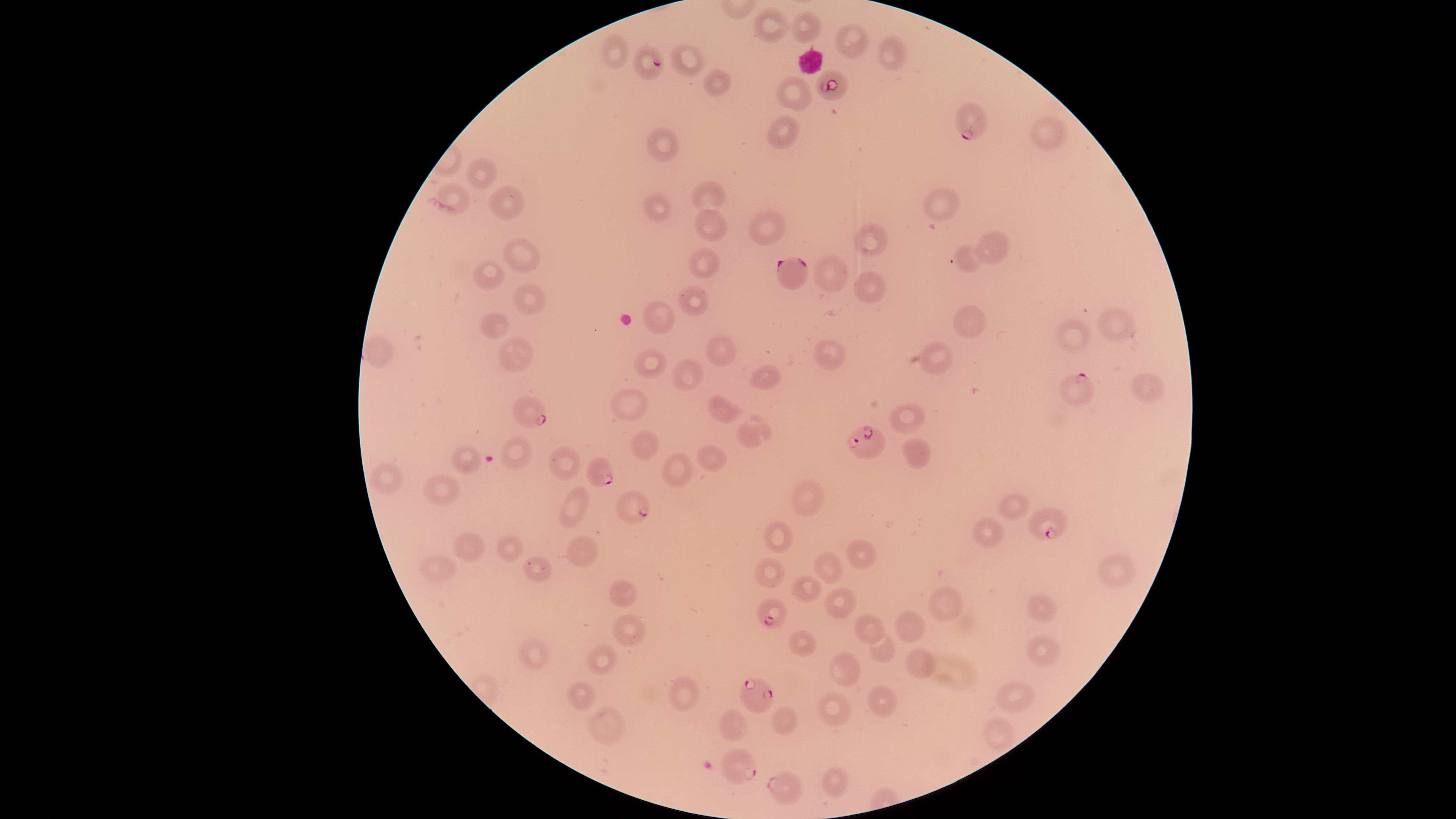
image size = 1456×819 pixels
capture = smartphone photograph through the microscope eyepiece
uninfected RBCs = approximate marker points as [x, y] in pixels: [801, 27], [763, 31], [847, 43], [617, 54], [885, 54], [688, 61], [713, 82], [792, 92], [780, 130], [1047, 130], [663, 145], [477, 181], [708, 192], [503, 204], [945, 208], [655, 214], [708, 223], [763, 228], [992, 246], [869, 249], [524, 259], [706, 261], [969, 265], [487, 274], [836, 279], [867, 289], [530, 299], [694, 301], [964, 319], [660, 321], [1106, 329], [497, 330], [1072, 339], [723, 346], [834, 353], [935, 353], [518, 354], [650, 363], [690, 374], [763, 375], [1151, 385], [627, 404], [723, 409], [911, 417], [752, 428], [645, 446], [914, 454], [522, 455], [466, 458], [566, 462], [708, 462], [677, 474], [389, 480], [445, 488], [807, 498], [574, 500], [1008, 504], [986, 533], [778, 537], [510, 543], [472, 550], [858, 552], [581, 555], [537, 561], [438, 571], [825, 571], [773, 575], [1106, 576], [627, 589], [803, 590], [839, 600], [1044, 606], [944, 608], [870, 625], [911, 625], [631, 630], [801, 640], [880, 650], [1041, 650], [536, 656], [603, 660], [919, 660], [847, 670], [684, 692], [876, 695], [581, 698], [1013, 699], [833, 704], [604, 718], [785, 718], [731, 723], [996, 733], [833, 777]
field of view = single
visible region = circular
species = Plasmodium falciparum
parasitized RBCs = approximate marker points as [x, y] in pixels: [652, 63], [832, 87], [968, 121], [794, 272], [1075, 387], [535, 415], [868, 445], [600, 470], [636, 504], [1045, 527], [769, 614], [761, 690], [740, 766], [775, 787]
stain = Giemsa
preparation = thin smear of blood
presence = malaria parasites identified